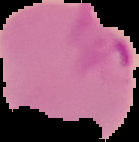
Summary:
  - Image type: segmented cell region with the area outside set to black
  - Image size: 139×142 pixels
  - Malaria status: parasitized
  - Preparation: thin blood smear